Give the position of every leukocyte visible.
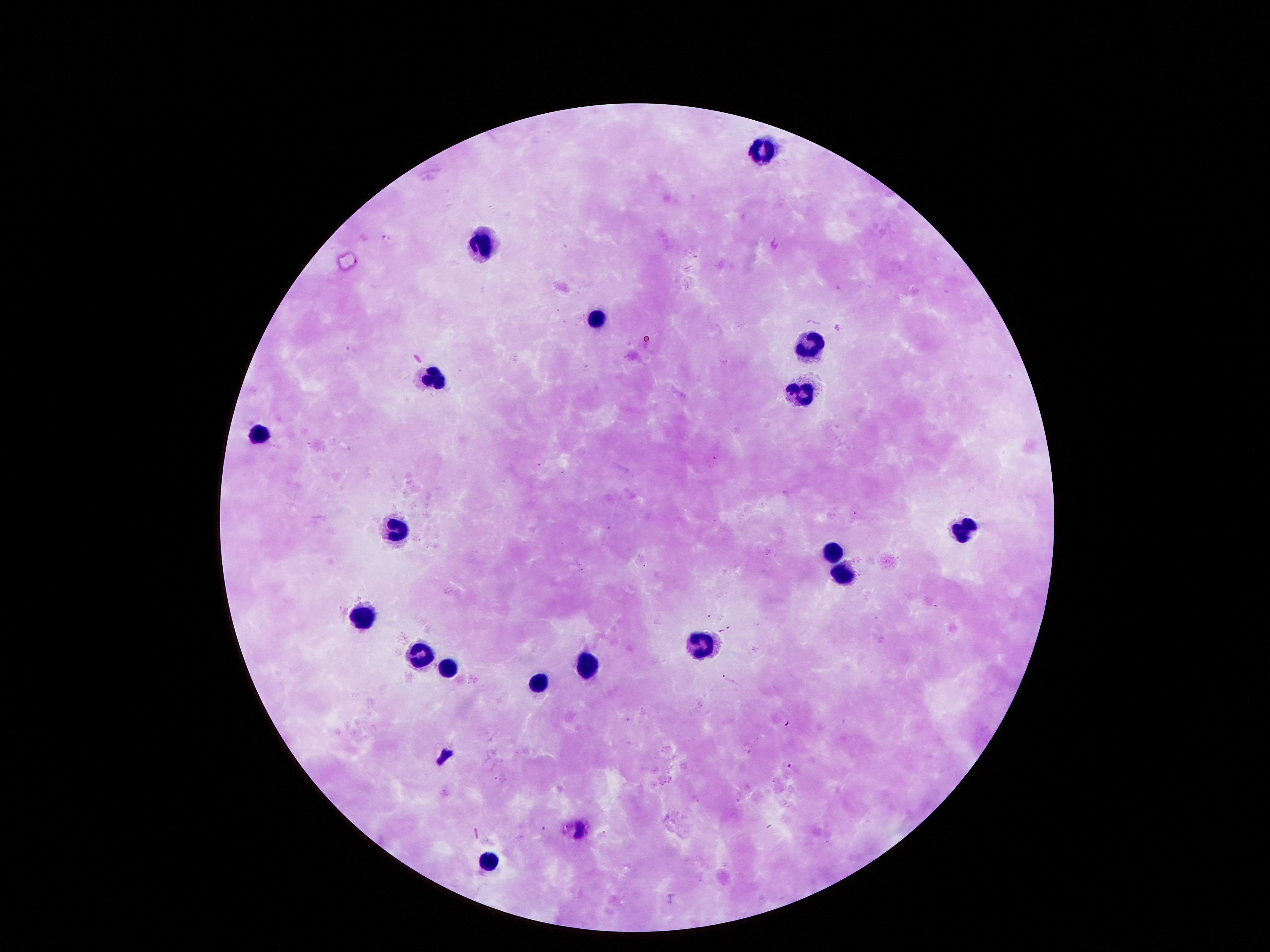
Approximate centers as {x, y} in pixels.
Leukocytes: {766, 146}, {477, 243}, {595, 317}, {803, 346}, {434, 374}, {803, 391}, {249, 437}, {397, 528}, {972, 532}, {834, 552}, {837, 571}, {363, 616}, {699, 648}, {417, 656}, {450, 669}, {585, 669}, {538, 682}, {487, 861}.

Summary:
  - Image size: 1270×952 pixels
  - Magnification: 100x
  - Patient malaria status: not infected
  - Field of view: one from this slide
  - Preparation: thick blood smear
  - Stain: Giemsa
  - Capture: smartphone camera through the microscope eyepiece